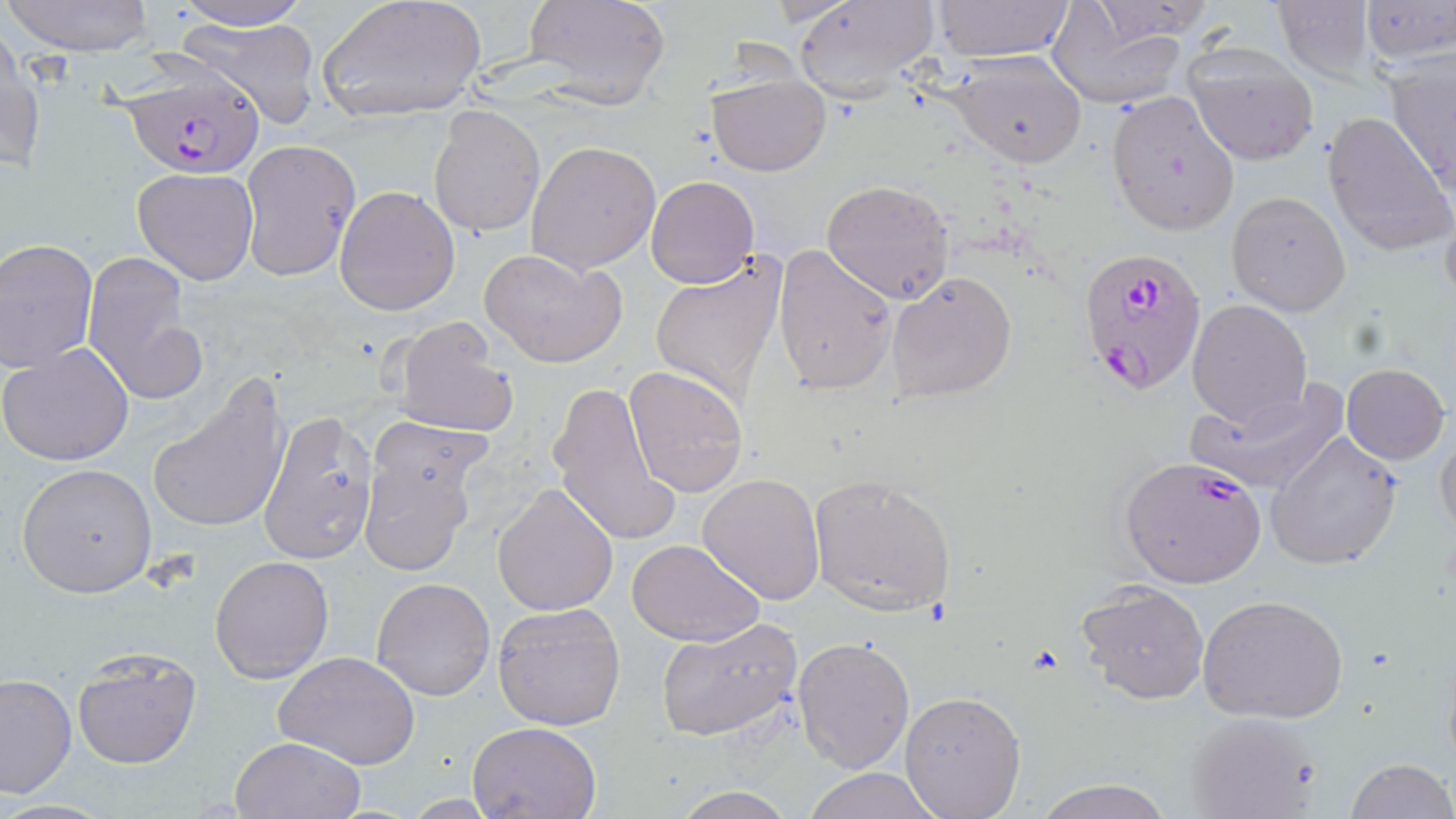
Approximate bounding boxes as (x1,y1)-(x2,y2) corner pairs in pixels. Plasmodium falciparum-infected red blood cell locations: (121,67)-(268,180), (1078,247)-(1208,397), (1119,454)-(1270,588). Uninfected red blood cell locations: (4,0)-(155,57), (169,0)-(314,30), (316,0)-(488,124), (522,0)-(670,110), (792,0)-(940,101), (932,0)-(1075,61), (1358,0)-(1456,68), (1272,1)-(1380,84), (1048,4)-(1188,110), (177,15)-(323,128), (0,27)-(43,176), (1181,41)-(1320,166), (944,48)-(1090,169), (1386,53)-(1455,195), (707,70)-(829,176), (1105,91)-(1240,235), (428,106)-(546,238), (1322,110)-(1454,256), (524,140)-(660,274), (239,141)-(359,279), (132,167)-(258,284), (646,176)-(759,288), (822,178)-(954,303), (334,184)-(459,317), (1439,189)-(1456,317), (1225,190)-(1352,316), (0,239)-(99,370), (773,243)-(897,396), (480,247)-(626,368), (84,249)-(206,406), (649,256)-(788,400), (887,270)-(1019,402), (1186,299)-(1312,428), (390,315)-(519,438), (0,341)-(133,465), (1340,363)-(1450,465), (623,365)-(748,497), (147,378)-(292,536), (548,380)-(679,547), (1187,383)-(1348,497), (258,412)-(378,564), (366,416)-(495,516), (1435,427)-(1456,542), (1263,433)-(1404,570), (360,450)-(478,575), (15,463)-(157,597), (697,473)-(826,605), (808,473)-(957,616), (492,481)-(618,616), (627,536)-(765,648), (209,555)-(334,684), (371,576)-(495,701), (1076,579)-(1210,704), (1198,594)-(1349,725), (492,602)-(626,730), (654,618)-(803,743), (793,636)-(915,772), (71,648)-(202,769), (275,652)-(421,769), (0,672)-(76,799), (900,691)-(1026,818), (1182,709)-(1322,817), (469,719)-(602,819), (229,736)-(366,819), (1344,758)-(1454,819), (801,767)-(944,819), (1034,778)-(1173,819), (671,788)-(800,819). Slide-level diagnosis: Plasmodium falciparum. May-Grünwald-Giemsa stain. Thin blood smear. Optical microscopy. Single field of view. Image is 1456×819 pixels. 1000x magnification.